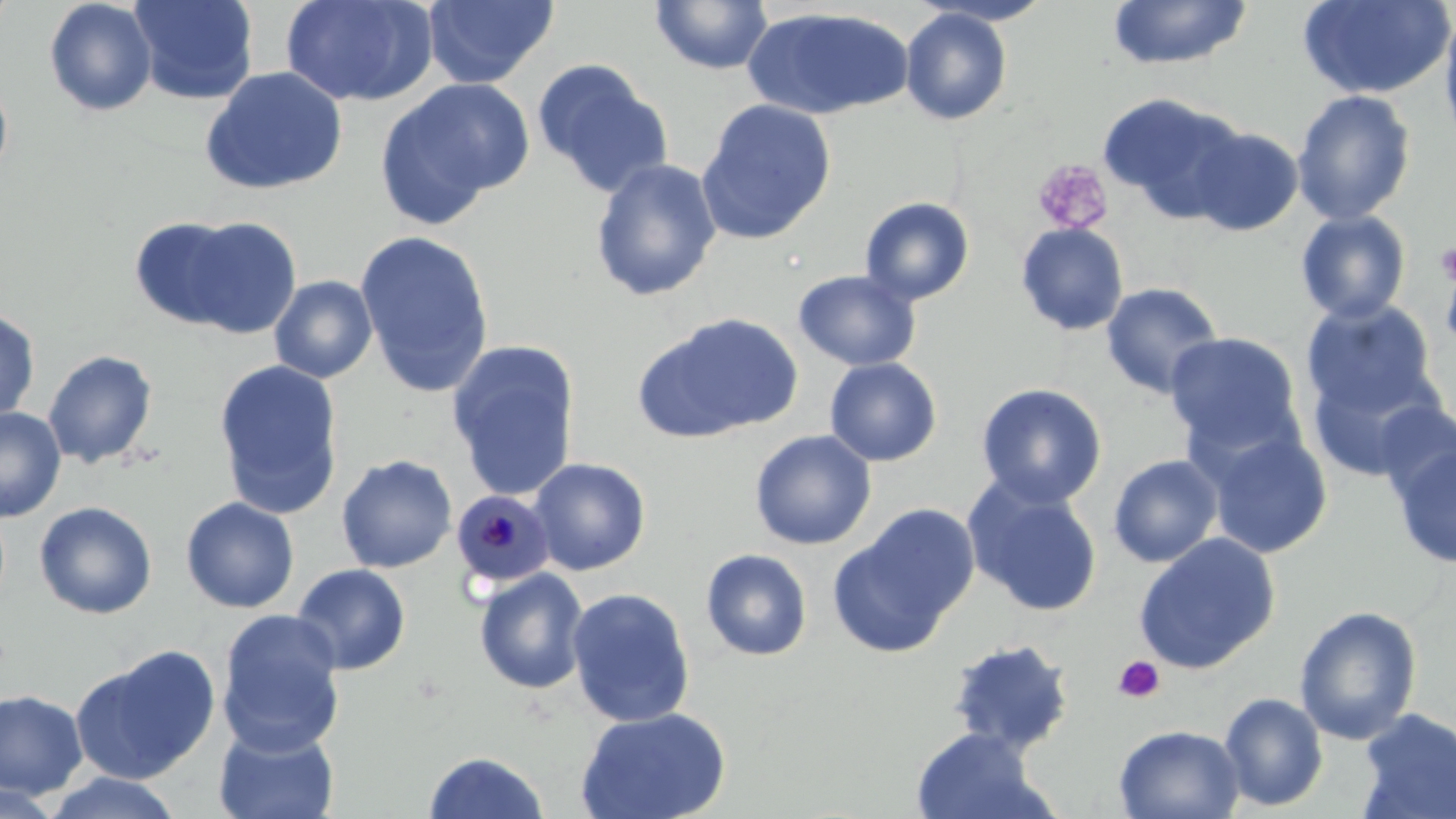
slide-level diagnosis = Plasmodium malariae
magnification = 1000x
uninfected red blood cell locations = approximate bounding boxes as (x1,y1)-(x2,y2) corner pairs in pixels: (43,0)-(158,116), (129,0)-(259,104), (279,0)-(437,108), (422,0)-(559,89), (1107,0)-(1252,70), (1297,0)-(1455,100), (649,1)-(774,75), (919,1)-(1056,26), (743,7)-(912,120), (900,8)-(1013,126), (1438,8)-(1456,151), (532,59)-(673,198), (200,66)-(349,196), (0,75)-(14,182), (376,78)-(533,225), (1292,89)-(1416,225), (1097,92)-(1245,220), (697,99)-(837,243), (1186,125)-(1303,236), (590,158)-(723,302), (859,196)-(975,306), (1294,210)-(1412,324), (169,215)-(302,339), (128,216)-(251,329), (1015,222)-(1129,336), (355,230)-(495,397), (1438,248)-(1456,363), (793,269)-(921,371), (269,275)-(379,383), (1100,282)-(1224,400), (1301,298)-(1439,421), (0,307)-(41,424), (636,311)-(803,443), (1165,331)-(1306,460), (445,340)-(581,502), (43,349)-(158,469), (824,357)-(942,467), (213,359)-(344,519), (1304,361)-(1440,483), (975,383)-(1107,508), (1374,401)-(1455,506), (0,406)-(66,522), (749,429)-(877,551), (1205,429)-(1333,559), (1389,438)-(1456,571), (336,454)-(457,573), (1108,454)-(1224,568), (528,457)-(651,576), (964,479)-(1104,618), (180,496)-(300,613), (33,501)-(157,619), (829,505)-(980,658), (1132,532)-(1281,675), (700,548)-(813,662), (291,563)-(411,675), (474,567)-(590,695), (565,587)-(696,727), (1293,605)-(1423,745), (216,610)-(346,756), (947,637)-(1076,754), (70,645)-(220,784), (0,689)-(88,798), (1218,692)-(1328,811), (574,706)-(731,819), (1354,707)-(1456,819), (1113,724)-(1246,819), (214,725)-(340,819), (911,727)-(1050,818), (423,750)-(549,818), (42,771)-(186,818), (0,780)-(68,819)
preparation = thin blood smear
field of view = single
stain = May-Grünwald-Giemsa
platelet locations = approximate bounding boxes as (x1,y1)-(x2,y2) corner pairs in pixels: (1032,160)-(1114,236), (1435,240)-(1456,286), (1114,655)-(1166,703)
modality = optical microscopy
Plasmodium malariae-infected red blood cell locations = approximate bounding boxes as (x1,y1)-(x2,y2) corner pairs in pixels: (450,489)-(555,590)
image size = 1456×819 pixels